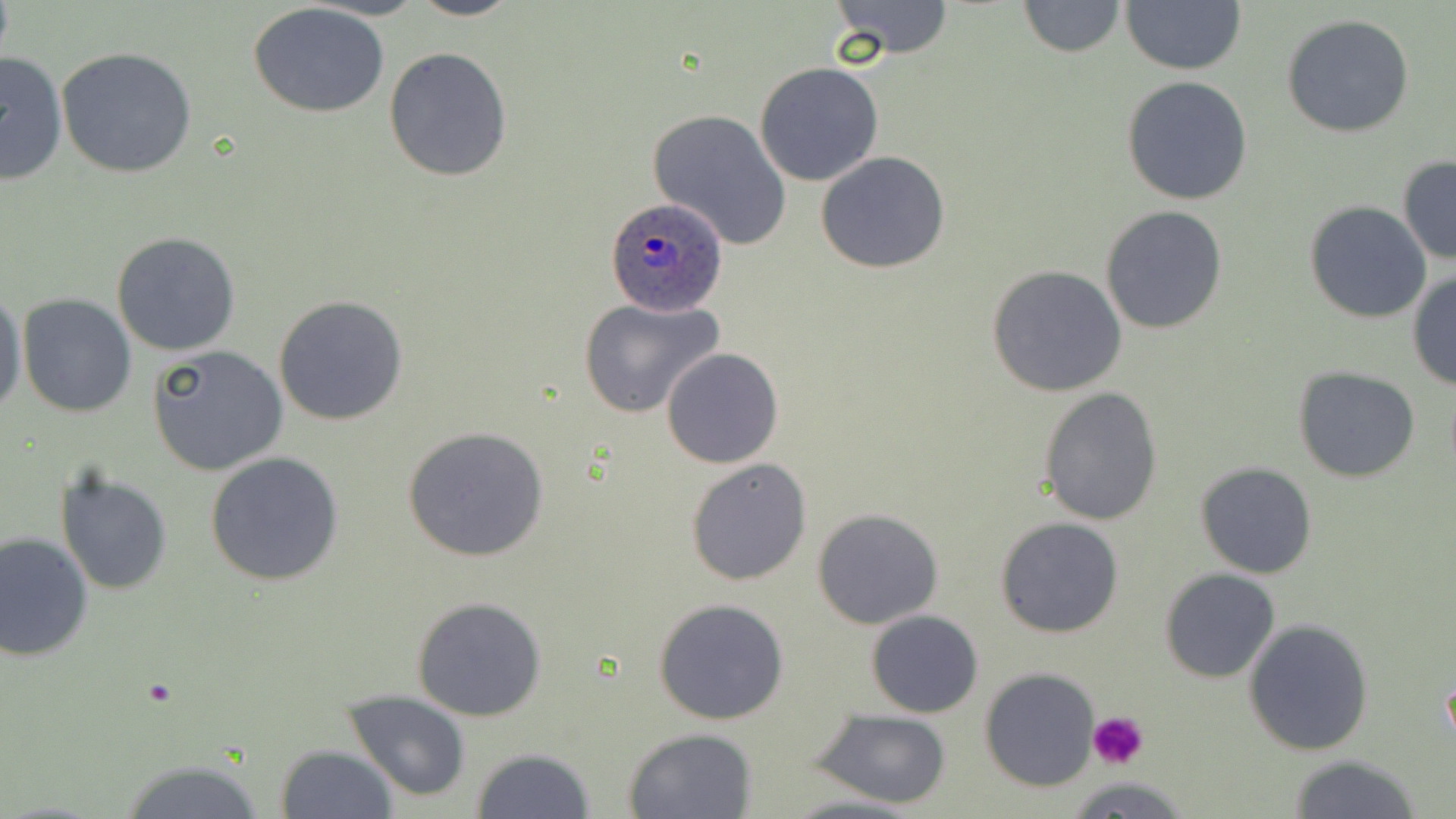
Summary:
  - Coordinate format: approximate bounding boxes as (x1, y1, x2, y2) in pixels
  - Uninfected red blood cell locations: (406, 0, 522, 22), (829, 0, 957, 58), (1016, 0, 1126, 56), (1121, 0, 1246, 74), (247, 3, 391, 117), (1281, 15, 1415, 138), (384, 45, 514, 182), (57, 46, 200, 179), (0, 49, 70, 183), (755, 61, 885, 186), (1121, 76, 1253, 206), (648, 108, 793, 251), (815, 152, 952, 274), (1397, 156, 1455, 266), (1304, 202, 1433, 323), (1100, 205, 1227, 334), (110, 231, 241, 357), (985, 264, 1128, 397), (1407, 270, 1456, 390), (0, 284, 26, 419), (18, 294, 136, 418), (274, 295, 408, 426), (578, 296, 724, 418), (147, 344, 287, 476), (661, 346, 784, 468), (1294, 367, 1421, 481), (1038, 386, 1163, 525), (401, 424, 553, 562), (205, 451, 345, 586), (686, 457, 812, 585), (1195, 460, 1318, 578), (55, 468, 174, 595), (811, 508, 945, 629), (994, 517, 1124, 638), (0, 530, 94, 662), (1159, 569, 1280, 683), (411, 595, 548, 721), (653, 597, 788, 725), (865, 610, 983, 718), (1243, 618, 1373, 757), (980, 669, 1102, 792), (344, 690, 473, 802), (812, 710, 953, 807), (622, 728, 757, 817), (276, 743, 397, 818), (469, 747, 596, 819), (1287, 755, 1425, 818), (112, 758, 275, 817), (777, 792, 928, 819)
  - Platelet locations: (1085, 712, 1149, 769)
  - Plasmodium ovale-infected red blood cell locations: (601, 196, 731, 315)
  - Slide-level diagnosis: Plasmodium ovale
  - Modality: optical microscopy
  - Stain: May-Grünwald-Giemsa
  - Magnification: 1000x
  - Preparation: thin blood smear
  - Field of view: one of a larger specimen
  - Image size: 1456×819 pixels